Comment on the morphology of the erythrocytes.
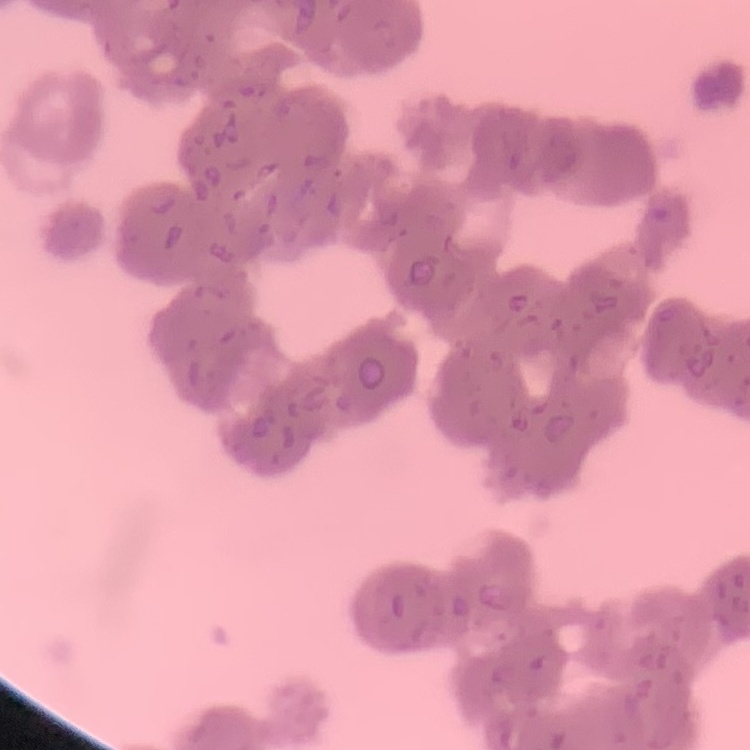
Rouleaux formation.

image type = one tile cut from a larger photomicrograph
preparation = thin blood smear
stain = Field's or Giemsa